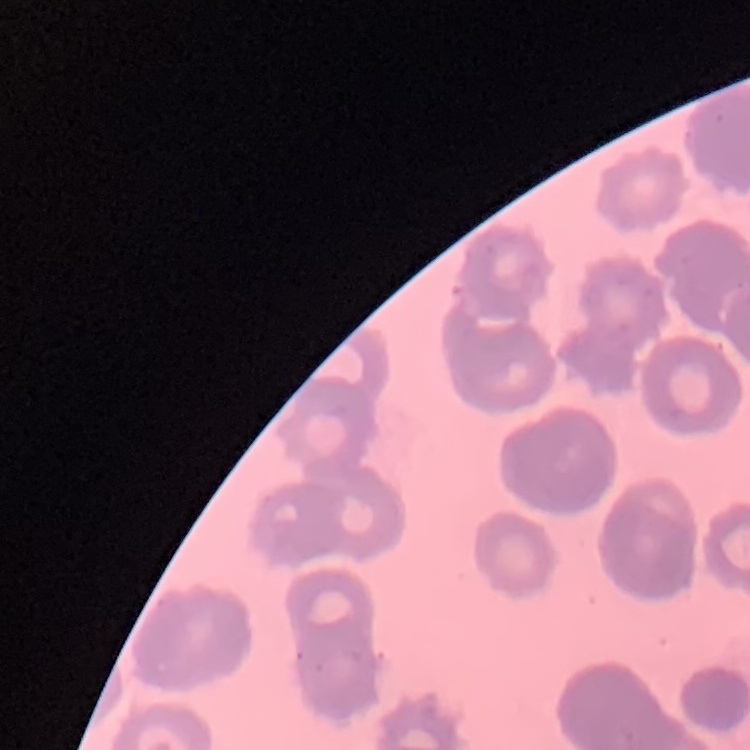

Summary:
  - Red blood cell morphology: rouleaux formation
  - Stain: Field's or Giemsa
  - Preparation: thin peripheral smear
  - Image type: one tile cut from a larger photomicrograph